Outline Plasmodium falciparum parasites and classify them by life-cycle stage.
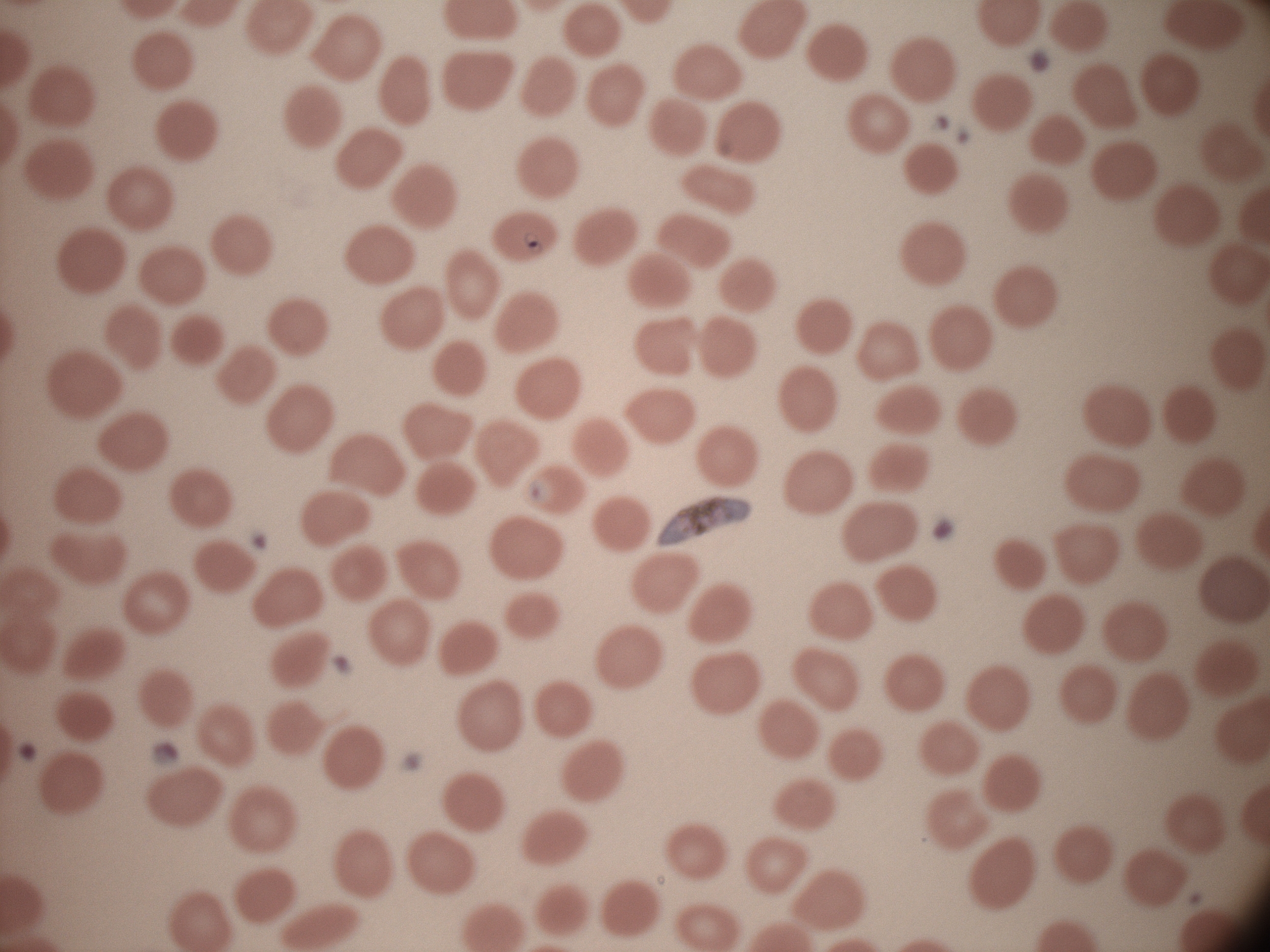

Approximate bounding boxes as named x1/y1/x2/y2 corners in pixels, from the source annotation, which is not necessarily exhaustive.
Trophozoites: (x1=524, y1=233, x2=542, y2=254).
Gametocytes: (x1=658, y1=495, x2=752, y2=547).

Summary:
  - Life-cycle stages among the annotated parasites: trophozoite, gametocyte
  - Field of view: one from this slide
  - Microscope: Leica DM2000 with built-in camera
  - Magnification: 100x
  - Species: Plasmodium falciparum
  - Image size: 1270×952 pixels
  - Stain: Giemsa
  - Preparation: thin blood film